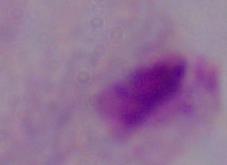

Summary:
  - Modality: micrograph
  - Identification: trichomonad
  - Magnification: 1000x